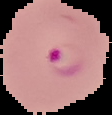

{
  "preparation": "thin blood film",
  "image_type": "segmented cell region with the area outside set to black",
  "result": "malaria parasites identified",
  "image_size": "112×115 pixels"
}